Locate Plasmodium parasites and leukocytes.
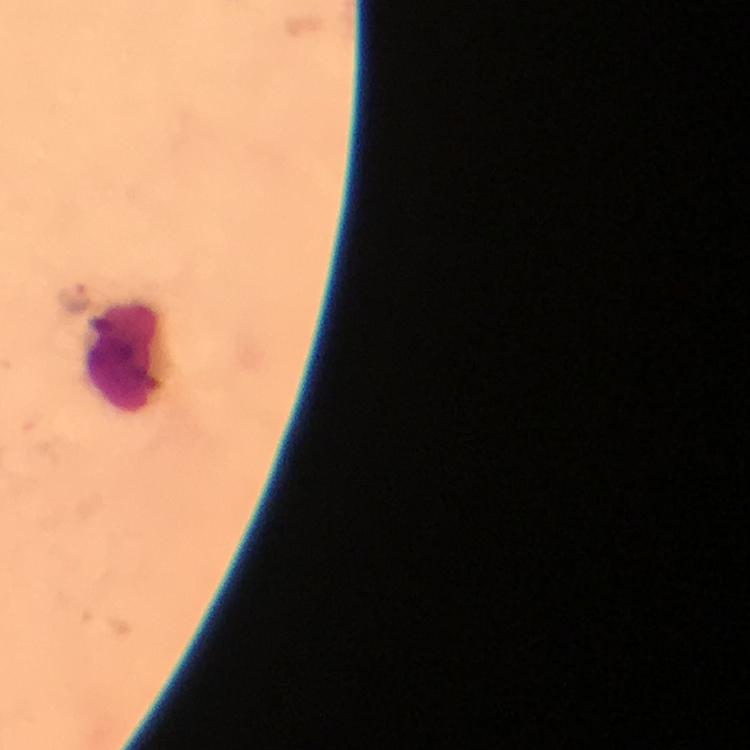
Approximate centers as [x, y] in pixels.
Plasmodium parasites: [72, 298].
Leukocytes: [125, 353].

Summary:
  - Context: from a malaria diagnostic workup
  - Capture: smartphone photograph through a microscope
  - Immersion oil: used
  - Preparation: thick smear
  - Stain: Giemsa
  - Magnification: 100x
  - Cropped from: a single field of view
  - Image size: 750×750 pixels